Name the parasite shown.
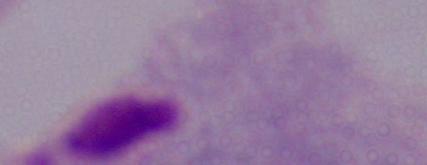

A trichomonad.

1000x magnification. Micrograph.